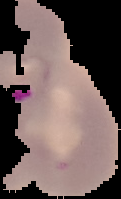
image size = 121×199 pixels
result = malaria parasites detected
image type = segmented cell region on a black background
preparation = thin blood film